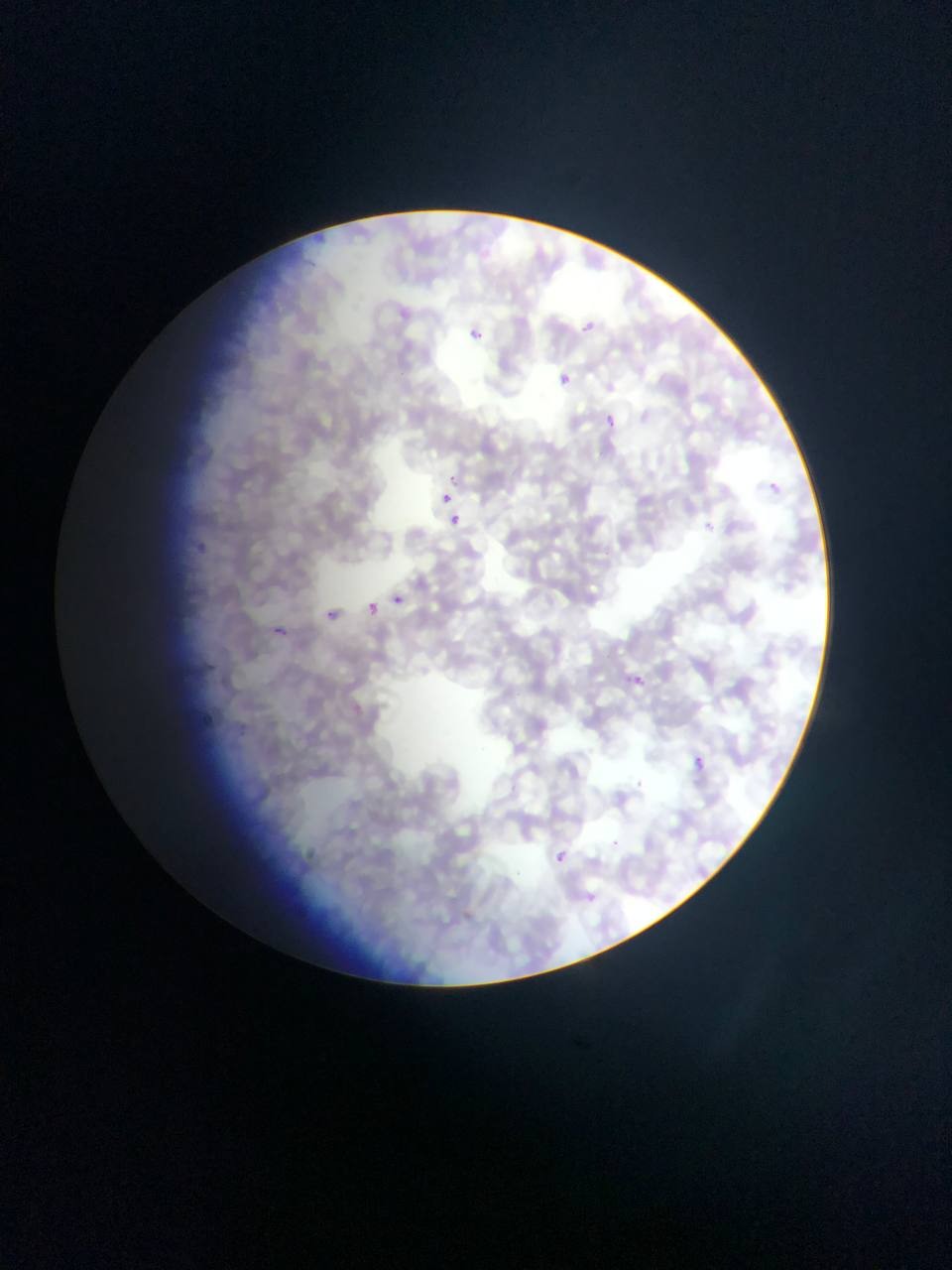

Approximate bounding boxes as (left, top, right, bottom) in pixels.
Summary:
  - Plasmodium parasite locations: (570, 301, 608, 346), (463, 322, 503, 372), (544, 367, 577, 385), (604, 413, 617, 427), (443, 494, 452, 505), (450, 515, 460, 525), (394, 596, 404, 604), (367, 603, 377, 615), (326, 610, 335, 618), (275, 626, 286, 634), (693, 757, 706, 771), (545, 842, 581, 873)
  - Country: Ghana
  - Image size: 952×1270 pixels
  - Field of view: single
  - Capture: mobile-phone photograph through a microscope
  - Preparation: thin blood smear